Identify the parasite.
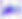

This is Toxoplasma gondii.

Summary:
  - Modality: micrograph
  - Magnification: 400x